State the blood parasite species.
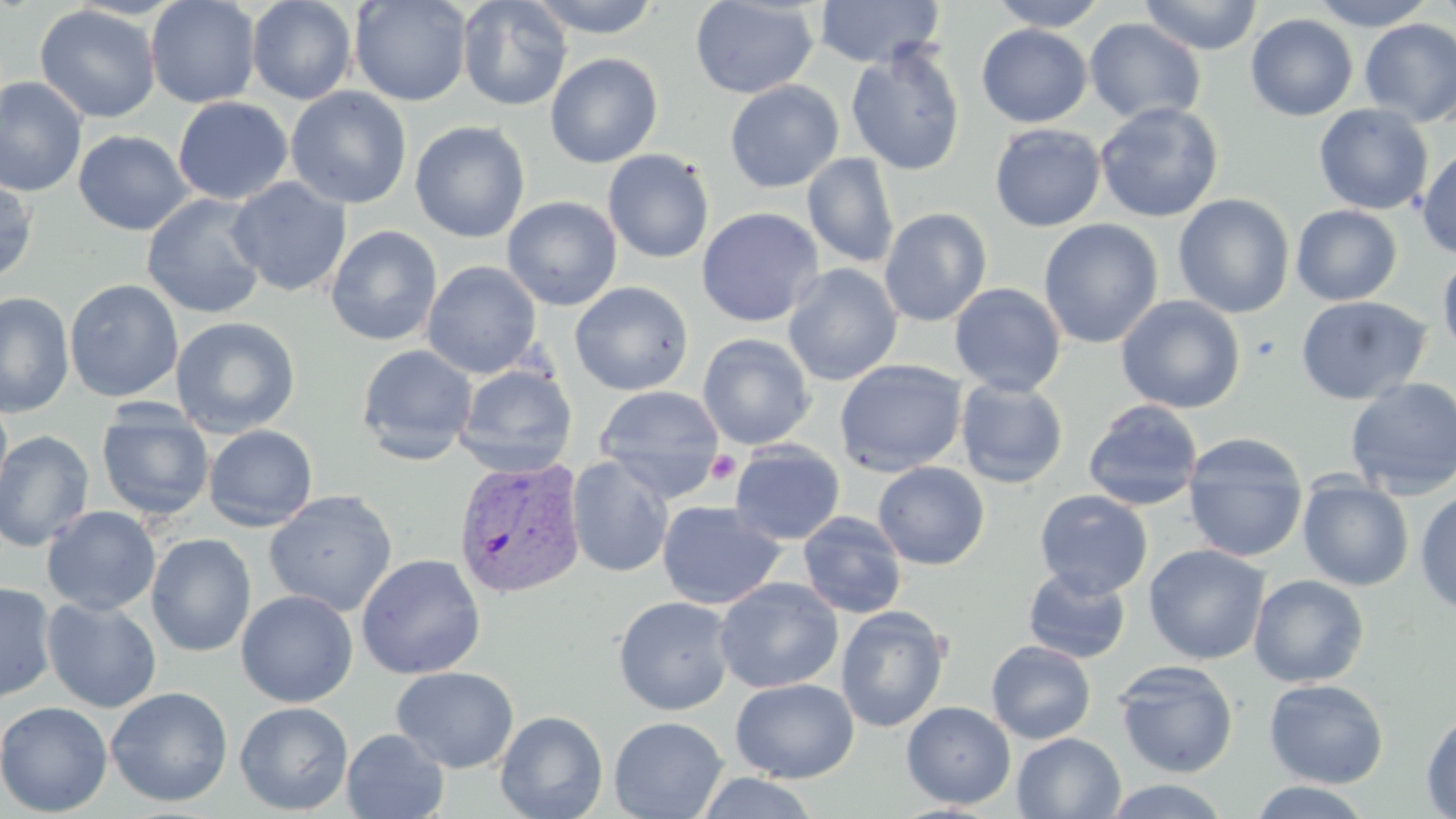

Plasmodium vivax.

Approximate bounding boxes as [x1, y1, x2, y2] in pixels. Platelet locations: [706, 451, 740, 484]. Uninfected red blood cell locations: [145, 0, 261, 109], [246, 0, 358, 105], [349, 0, 473, 107], [456, 0, 573, 111], [526, 0, 664, 38], [689, 0, 819, 99], [813, 0, 945, 68], [989, 0, 1108, 31], [1138, 0, 1263, 55], [1312, 0, 1434, 30], [1434, 0, 1456, 26], [35, 5, 160, 123], [1245, 13, 1358, 121], [1084, 18, 1206, 125], [1359, 18, 1456, 127], [976, 24, 1092, 128], [845, 43, 966, 176], [545, 52, 664, 168], [0, 77, 88, 198], [724, 80, 844, 193], [285, 87, 412, 209], [173, 97, 293, 205], [1094, 101, 1225, 223], [1313, 103, 1434, 216], [410, 120, 530, 243], [989, 124, 1106, 232], [73, 130, 194, 236], [1416, 146, 1456, 260], [602, 149, 715, 264], [802, 152, 899, 269], [0, 175, 38, 283], [226, 177, 352, 297], [141, 193, 268, 319], [1173, 193, 1295, 318], [502, 196, 622, 311], [1291, 204, 1402, 306], [696, 206, 824, 327], [879, 207, 992, 327], [1038, 218, 1163, 348], [325, 225, 443, 346], [1437, 251, 1456, 360], [422, 261, 542, 379], [783, 264, 903, 386], [64, 279, 184, 402], [569, 281, 694, 396], [949, 282, 1067, 396], [0, 291, 75, 418], [1116, 295, 1246, 414], [1295, 296, 1432, 405], [170, 316, 301, 437], [698, 333, 815, 450], [356, 344, 478, 465], [834, 359, 967, 477], [454, 364, 578, 477], [955, 378, 1069, 489], [1344, 378, 1456, 501], [593, 385, 725, 501], [0, 396, 13, 509], [1082, 399, 1204, 512], [96, 404, 214, 522], [203, 425, 318, 531], [0, 430, 95, 552], [1181, 434, 1309, 563], [729, 441, 846, 545], [567, 455, 675, 578], [873, 461, 990, 570], [1298, 477, 1414, 591], [1414, 488, 1456, 615], [1034, 489, 1153, 598], [263, 490, 397, 617], [657, 501, 785, 610], [42, 506, 161, 616], [798, 512, 908, 619], [146, 533, 257, 657], [1143, 543, 1270, 665], [356, 553, 486, 680], [1022, 566, 1132, 664], [1248, 574, 1370, 688], [714, 577, 844, 693], [0, 582, 57, 702], [236, 590, 358, 707], [613, 595, 737, 716], [41, 597, 162, 713], [835, 606, 950, 733], [986, 640, 1096, 744], [1113, 660, 1239, 778], [391, 666, 519, 773], [730, 678, 859, 783], [1264, 678, 1389, 788], [105, 686, 233, 808], [0, 700, 113, 817], [235, 701, 354, 816], [901, 701, 1016, 809], [495, 710, 608, 819], [1421, 710, 1456, 817], [609, 716, 728, 819], [341, 728, 449, 819], [1012, 732, 1126, 818], [695, 771, 821, 818], [1101, 778, 1234, 818], [1247, 780, 1375, 818]. Plasmodium vivax-infected red blood cell locations: [452, 456, 587, 601]. May-Grünwald-Giemsa stain. Single field of view. Image is 1456×819 pixels. Thin blood smear. Optical microscopy. Captured at 1000x magnification.